Locate every blood parasite and identify its species.
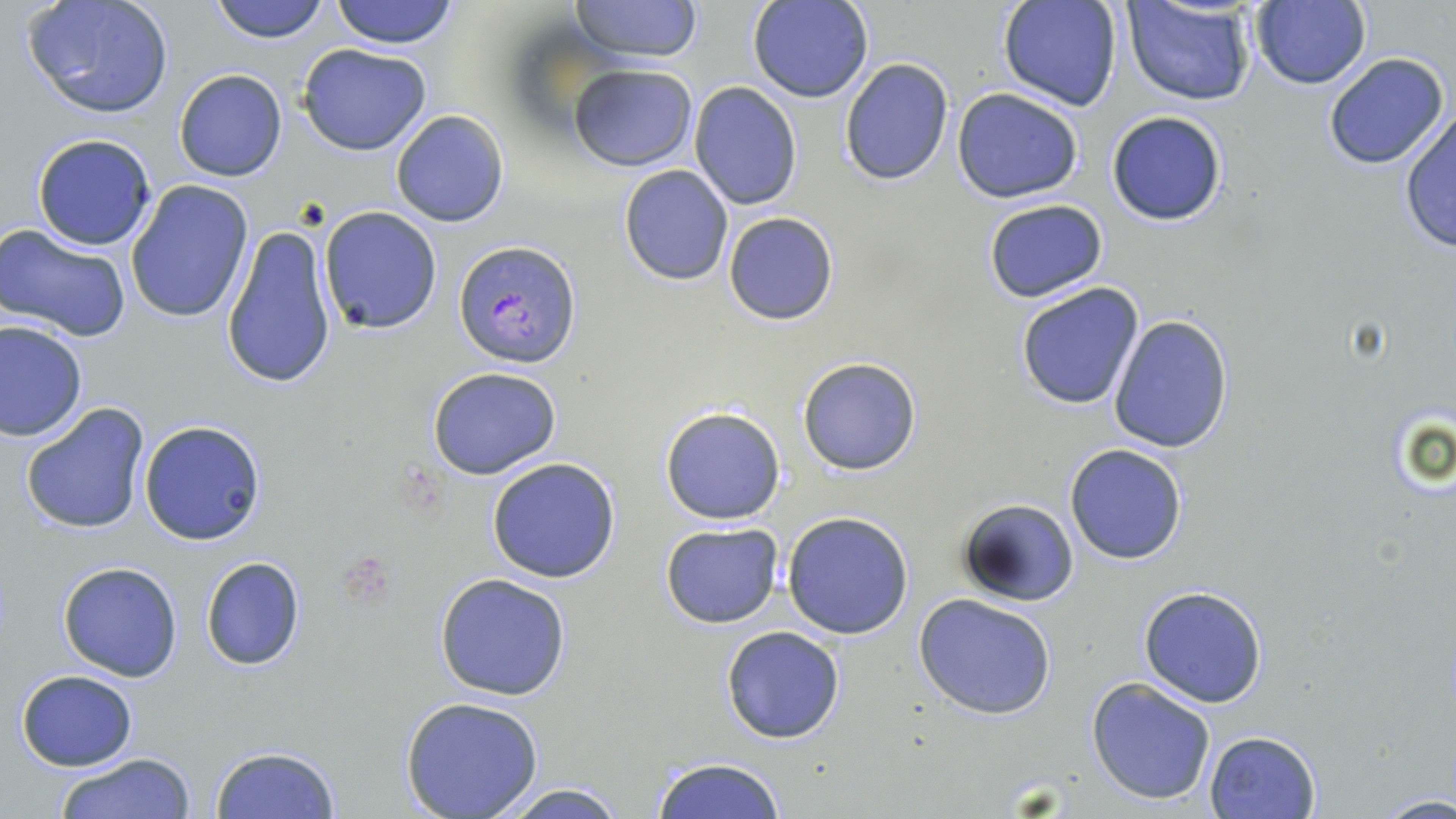
Approximate bounding boxes as (x1, y1, x2, y2) in pixels.
Plasmodium falciparum-infected red blood cells: (457, 240, 581, 369).
No Plasmodium ovale, Plasmodium malariae, Plasmodium vivax, Babesia divergens, or Trypanosoma brucei observed.

Uninfected red blood cell locations: (208, 0, 329, 44), (330, 0, 459, 48), (571, 0, 703, 63), (749, 0, 872, 103), (20, 1, 177, 121), (998, 1, 1123, 112), (1120, 2, 1257, 107), (1245, 2, 1372, 89), (298, 42, 431, 156), (1322, 52, 1451, 170), (839, 58, 954, 186), (569, 63, 698, 171), (173, 68, 287, 182), (689, 82, 803, 210), (952, 88, 1085, 204), (1398, 107, 1456, 254), (389, 110, 509, 227), (1105, 110, 1229, 227), (31, 133, 156, 250), (618, 166, 734, 285), (125, 180, 255, 325), (982, 198, 1109, 303), (318, 205, 442, 334), (723, 210, 838, 324), (0, 222, 132, 341), (222, 224, 338, 389), (1016, 282, 1146, 411), (1108, 313, 1235, 453), (1, 319, 87, 441), (797, 356, 922, 476), (426, 367, 563, 479), (20, 402, 150, 536), (659, 405, 786, 525), (139, 419, 267, 544), (1063, 443, 1188, 565), (485, 457, 621, 583), (955, 498, 1080, 607), (782, 511, 914, 640), (660, 523, 783, 629), (201, 556, 306, 671), (58, 562, 182, 681), (434, 571, 573, 701), (1137, 585, 1267, 708), (913, 594, 1058, 721), (721, 625, 846, 745), (16, 669, 138, 771), (1087, 677, 1217, 806), (399, 697, 543, 818), (1205, 730, 1320, 819), (210, 745, 343, 819), (53, 752, 197, 819), (650, 758, 789, 818), (488, 781, 633, 819), (1374, 793, 1455, 818). Slide-level diagnosis: Plasmodium falciparum. Single field of view. Thin blood film. Image is 1456×819 pixels. 1000x magnification. May-Grünwald-Giemsa stain. Light microscopy.